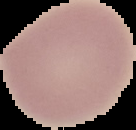
preparation = thin blood smear
image type = segmented cell region on a black background
malaria status = uninfected
image size = 136×130 pixels